Describe the morphology of the erythrocytes.
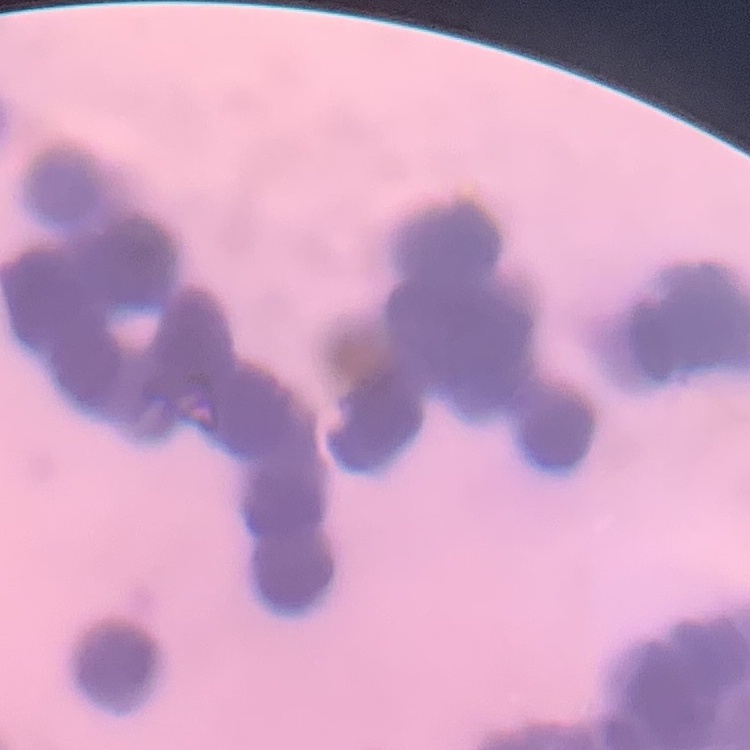
They show rouleaux formation.

Summary:
  - Image type: one tile cut from a larger photomicrograph
  - Stain: Field's or Giemsa
  - Preparation: thin blood film